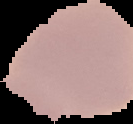
image type = segmented cell region on a black background
image size = 133×124 pixels
malaria status = uninfected
preparation = thin blood smear